Report the malaria status of this cell.
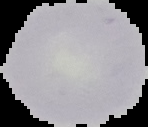

Uninfected.

preparation: thin blood film
image_size: 148×127 pixels
image_type: segmented cell region on a black background